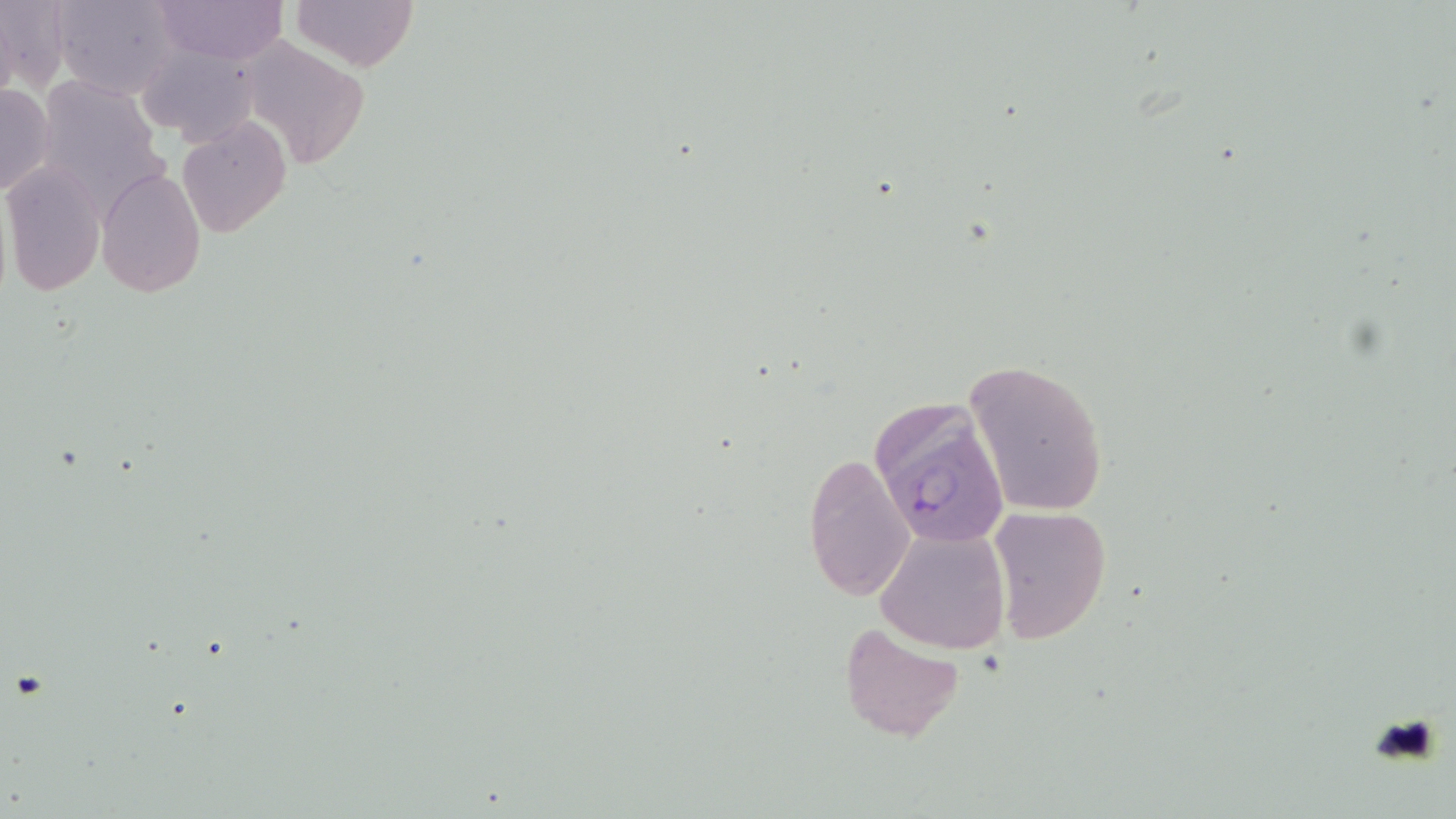

Summary:
  - Coordinate format: approximate bounding boxes as named x1/y1/x2/y2 corners in pixels
  - Uninfected red blood cell locations: (x1=0, y1=0, x2=71, y2=94), (x1=49, y1=0, x2=180, y2=100), (x1=154, y1=0, x2=284, y2=64), (x1=288, y1=0, x2=418, y2=72), (x1=237, y1=37, x2=372, y2=170), (x1=135, y1=41, x2=263, y2=148), (x1=35, y1=76, x2=164, y2=209), (x1=1, y1=82, x2=55, y2=198), (x1=177, y1=117, x2=291, y2=238), (x1=1, y1=160, x2=107, y2=298), (x1=96, y1=168, x2=206, y2=298), (x1=965, y1=357, x2=1110, y2=519), (x1=803, y1=451, x2=914, y2=601), (x1=985, y1=505, x2=1111, y2=645), (x1=874, y1=526, x2=1010, y2=655), (x1=837, y1=621, x2=966, y2=741)
  - Plasmodium falciparum-infected red blood cell locations: (x1=865, y1=397, x2=1013, y2=555)
  - Slide-level diagnosis: Plasmodium falciparum
  - Modality: light microscopy
  - Image size: 1456×819 pixels
  - Magnification: 1000x
  - Stain: May-Grünwald-Giemsa
  - Preparation: thin blood film
  - Field of view: one of a larger specimen